Report the malaria status of this cell.
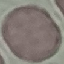

It is uninfected.

Thin blood film. Automatically extracted cell patch, resized to 64 × 64 pixels. Acquired by smartphone through the microscope eyepiece. Giemsa stain.